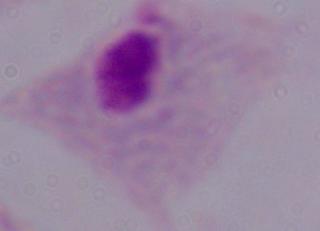

magnification: 1000x
identification: trichomonad
modality: micrograph